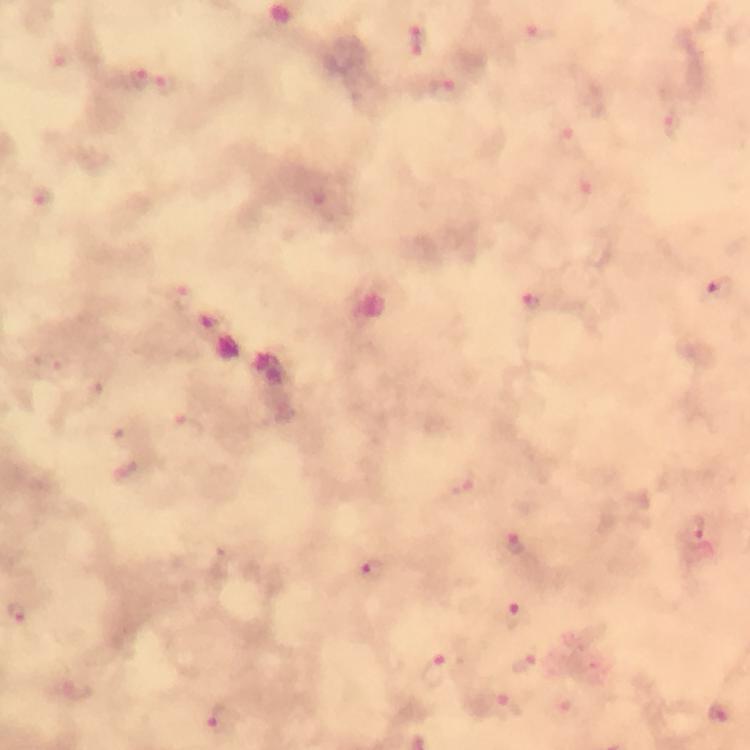

malaria parasite locations = approximate centers as (x, y) in pixels: (546, 36), (417, 38), (139, 78), (168, 85), (445, 92), (674, 125), (42, 200), (718, 292), (185, 299), (539, 302), (214, 326), (189, 427), (694, 529), (515, 546), (372, 570), (16, 614), (519, 617), (526, 664), (441, 669), (505, 709), (723, 712), (223, 719)
image size = 750×750 pixels
cropped from = one field of view
stain = Giemsa
magnification = 100x
capture = smartphone photograph through a microscope
context = from a diagnostic examination for malaria
immersion oil = used
preparation = thick blood film